Locate malaria parasites and leukocytes.
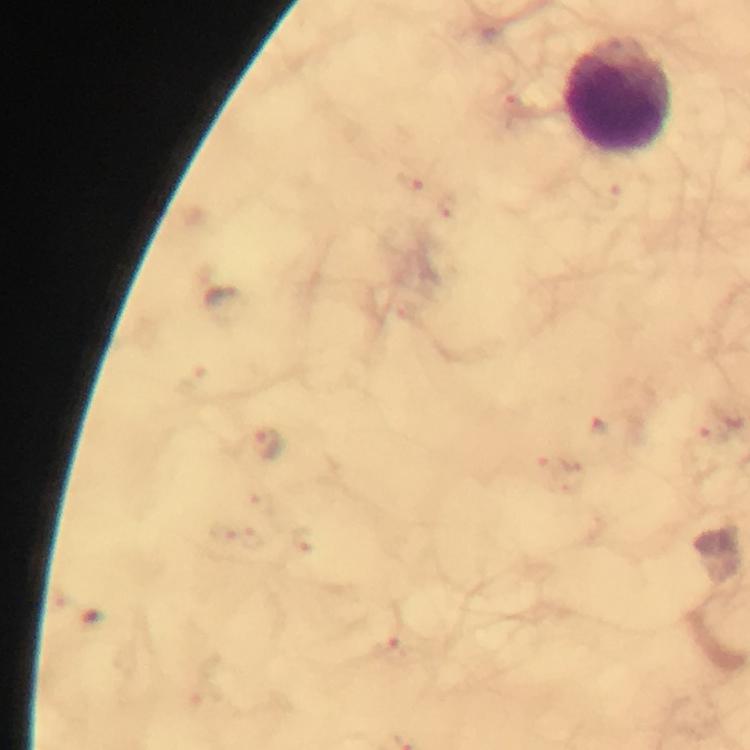

Approximate centers as [x, y] in pixels.
Malaria parasites: [227, 303], [267, 445].
Leukocytes: [620, 98].

From a diagnostic examination for malaria. At 100x magnification. Image is 750×750 pixels. Cropped region of a single field of view. Giemsa stain. Immersion oil applied. Thick blood film. Smartphone photograph taken through a microscope.